Which red blood cells are P. falciparum-infected, and which are of indeterminate infection status?
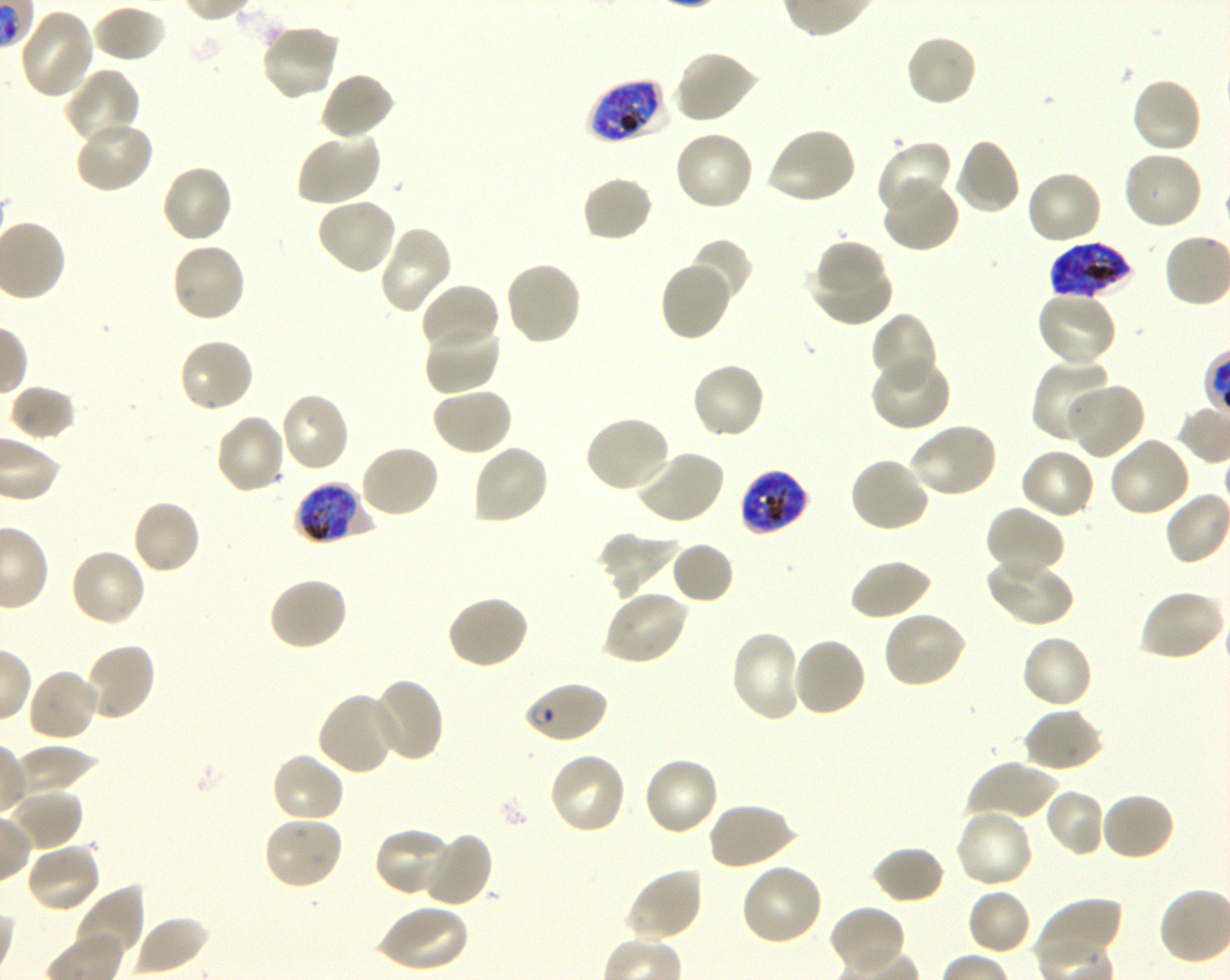

Approximate bounding boxes as {x1, y1, x2, y2} in pixels. Not every red blood cell is marked. A life-cycle stage — or a range of stages, where the recorded stages span more than one — follows each staged infected red blood cell.
Infected red blood cells: {586, 77, 668, 144} late trophozoite to late schizont; {1049, 242, 1138, 300} late trophozoite to late schizont; {738, 469, 809, 536} late trophozoite to late schizont; {294, 482, 371, 545} late trophozoite to late schizont; {522, 680, 608, 744} ring.
No red blood cells of indeterminate infection status observed.

{
  "locations_of_uninfected_red_blood_cells": "{91, 4, 167, 64}, {19, 7, 96, 99}, {261, 22, 342, 102}, {904, 33, 979, 108}, {673, 49, 759, 124}, {64, 68, 141, 146}, {319, 70, 396, 140}, {1130, 76, 1203, 155}, {74, 119, 155, 195}, {765, 127, 858, 206}, {673, 130, 755, 212}, {295, 131, 381, 207}, {952, 137, 1021, 216}, {874, 140, 952, 216}, {1121, 151, 1203, 232}, {160, 163, 234, 244}, {1024, 170, 1103, 246}, {581, 175, 654, 243}, {880, 179, 959, 254}, {315, 197, 399, 275}, {377, 228, 452, 316}, {689, 237, 752, 304}, {814, 239, 887, 300}, {170, 241, 248, 324}, {810, 257, 894, 325}, {659, 259, 733, 342}, {503, 260, 582, 347}, {419, 282, 500, 353}, {1035, 289, 1118, 369}, {870, 312, 937, 390}, {424, 320, 502, 395}, {177, 337, 256, 414}, {871, 355, 952, 433}, {1034, 359, 1114, 444}, {690, 361, 767, 441}, {1066, 382, 1145, 460}, {8, 384, 77, 442}, {430, 387, 514, 456}, {278, 391, 350, 473}, {214, 414, 287, 496}, {583, 415, 672, 494}, {909, 423, 999, 500}, {1108, 435, 1192, 518}, {358, 444, 440, 520}, {470, 444, 550, 526}, {1019, 447, 1096, 521}, {634, 448, 725, 526}, {848, 456, 930, 534}, {130, 498, 202, 575}, {985, 506, 1065, 577}, {598, 531, 680, 599}, {670, 541, 735, 605}, {68, 547, 147, 628}, {985, 554, 1073, 628}, {849, 558, 932, 621}, {267, 575, 349, 651}, {601, 590, 690, 666}, {1137, 590, 1226, 663}, {446, 593, 530, 670}, {881, 610, 969, 690}, {729, 629, 803, 722}, {1019, 633, 1094, 710}, {790, 636, 867, 718}, {84, 641, 157, 722}, {27, 667, 101, 744}, {367, 677, 445, 762}, {317, 691, 399, 776}, {1022, 705, 1104, 773}, {270, 751, 346, 824}, {547, 751, 628, 836}, {641, 756, 720, 838}, {967, 760, 1058, 824}, {1045, 787, 1106, 857}, {7, 788, 85, 852}, {1099, 792, 1176, 862}, {707, 801, 796, 870}, {953, 807, 1034, 889}, {262, 815, 345, 891}, {373, 827, 457, 898}, {421, 831, 494, 908}, {25, 841, 103, 914}, {870, 845, 946, 905}, {739, 862, 824, 947}, {624, 867, 704, 943}, {73, 884, 144, 963}, {966, 887, 1032, 956}, {1036, 896, 1122, 963}, {377, 903, 469, 973}, {828, 904, 907, 975}, {130, 919, 219, 976}",
  "objective": "100x, oil immersion, numerical aperture 1.30",
  "preparation": "thin blood film",
  "donor_blood_group": "O+",
  "image_size": "1230×980 pixels",
  "stain": "Giemsa",
  "field_of_view": "single",
  "culture": "in-vitro P. falciparum strain 3D7, shaking"
}